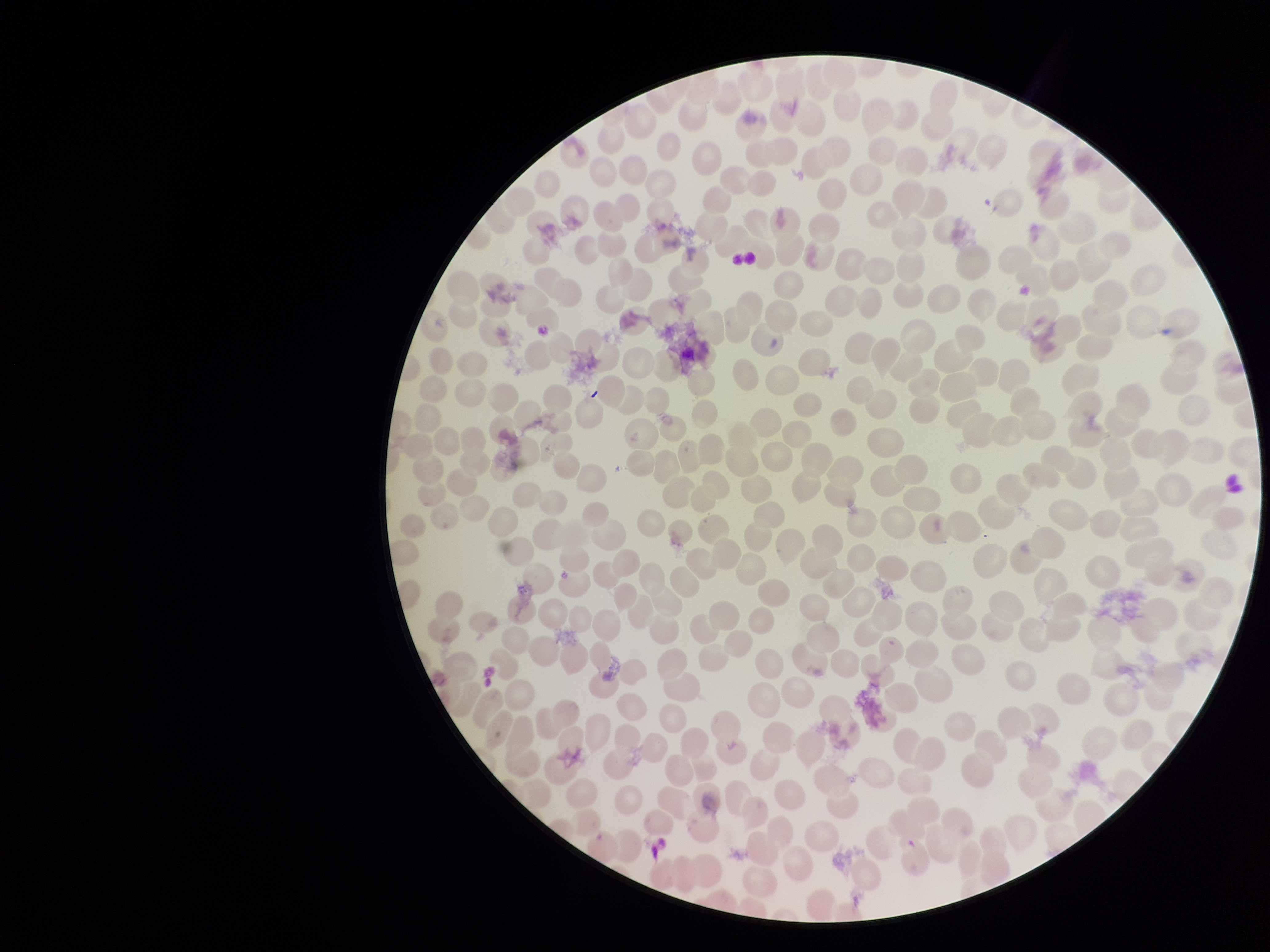

Summary:
  - Preparation: thin smear
  - Parasitized red blood cells: none detected
  - Stain: Giemsa
  - Parasitized red blood cell count: 0
  - Red blood cell count: 319
  - Field of view: single
  - Capture: smartphone photograph through the microscope eyepiece
  - Patient malaria status: negative
  - Image size: 1270×952 pixels